Comment on the morphology of the red blood cells.
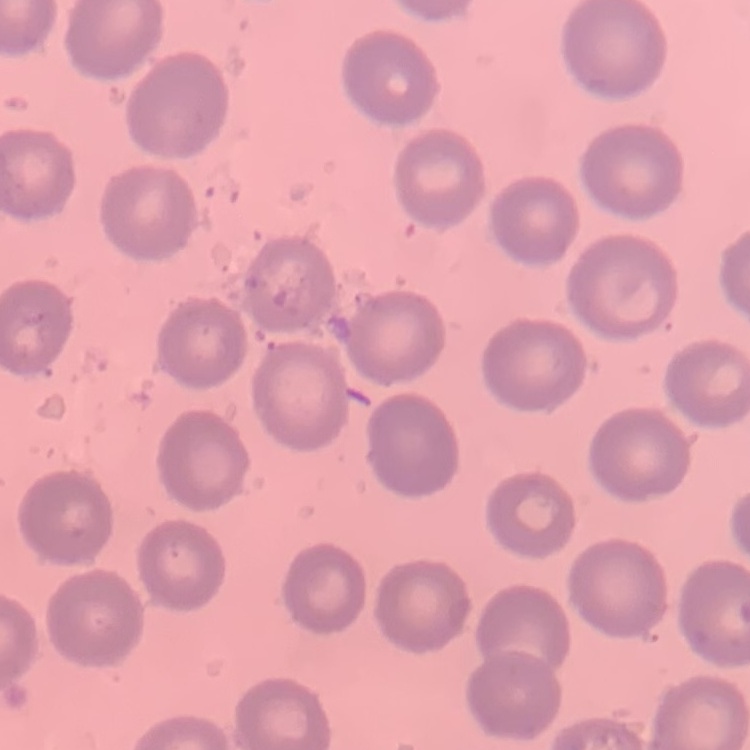
No rouleaux formation.

preparation = thin blood smear
stain = Field's or Giemsa
image type = one tile cut from a larger photomicrograph